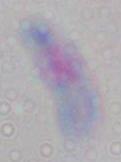
Toxoplasma gondii is shown. Micrograph. Captured at 1000x magnification.